Outline each Plasmodium malariae-infected red blood cell.
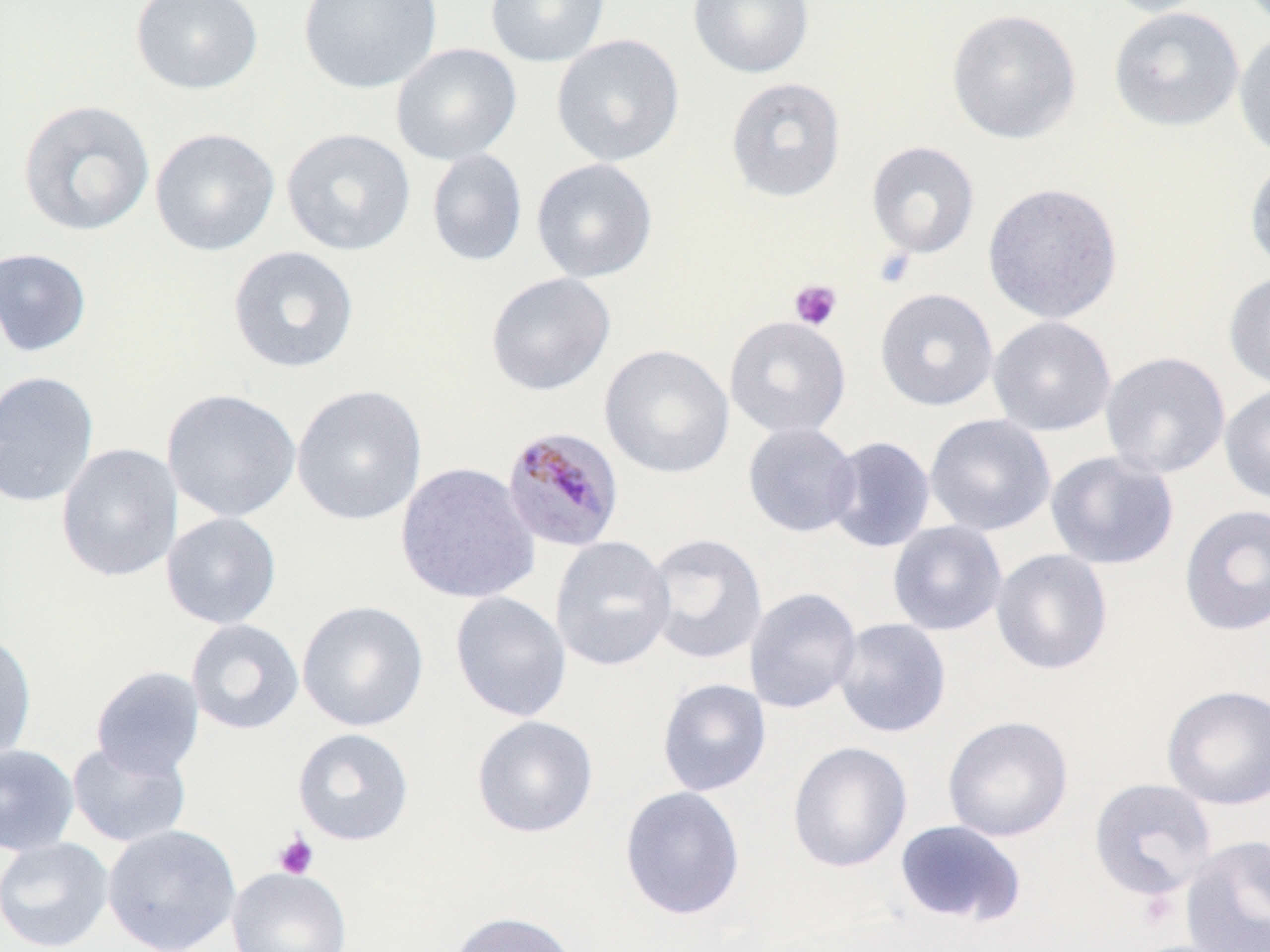
Approximate bounding boxes as [x1, y1, x2, y2] in pixels.
Plasmodium malariae-infected red blood cells: [500, 425, 625, 554].

Platelet locations: [873, 248, 916, 289], [789, 279, 842, 330], [273, 832, 318, 879]. Uninfected red blood cell locations: [130, 0, 263, 95], [297, 0, 442, 94], [485, 0, 610, 67], [687, 0, 814, 78], [1100, 0, 1220, 18], [1109, 6, 1245, 131], [946, 9, 1081, 144], [1233, 30, 1270, 160], [551, 34, 685, 167], [390, 43, 522, 165], [725, 77, 846, 203], [17, 100, 156, 237], [149, 127, 280, 256], [281, 128, 416, 256], [866, 141, 980, 259], [426, 148, 527, 267], [1244, 156, 1270, 276], [531, 158, 658, 283], [982, 182, 1123, 324], [227, 246, 360, 374], [0, 247, 92, 357], [485, 272, 616, 396], [1223, 272, 1270, 391], [874, 287, 998, 411], [724, 316, 851, 439], [987, 316, 1117, 436], [599, 344, 735, 478], [1100, 351, 1230, 479], [0, 370, 100, 509], [1220, 383, 1270, 505], [291, 384, 427, 526], [161, 388, 301, 523], [924, 414, 1056, 536], [742, 422, 861, 538], [824, 436, 936, 553], [56, 443, 182, 582], [1045, 450, 1179, 570], [395, 461, 540, 605], [1179, 503, 1270, 636], [160, 511, 282, 630], [887, 520, 1008, 636], [644, 533, 768, 665], [550, 536, 676, 672], [991, 548, 1114, 676], [743, 587, 862, 714], [449, 591, 572, 722], [296, 599, 430, 732], [185, 618, 305, 735], [833, 618, 952, 738], [0, 630, 37, 763], [90, 666, 205, 778], [656, 678, 772, 797], [1161, 684, 1270, 810], [471, 715, 599, 838], [942, 715, 1074, 842], [292, 727, 414, 846], [67, 740, 192, 848], [787, 741, 913, 873], [0, 743, 80, 856], [1088, 777, 1218, 901], [619, 785, 746, 921], [894, 820, 1027, 927], [102, 823, 242, 952], [1179, 835, 1270, 952], [0, 836, 114, 952], [227, 866, 352, 952], [446, 911, 579, 952]. Slide-level diagnosis: Plasmodium malariae. Optical microscopy. May-Grünwald-Giemsa-stained preparation. One field of a larger specimen. Thin blood smear. Captured at 1000x magnification. Image is 1270×952 pixels.